Locate every blood parasite and identify its species.
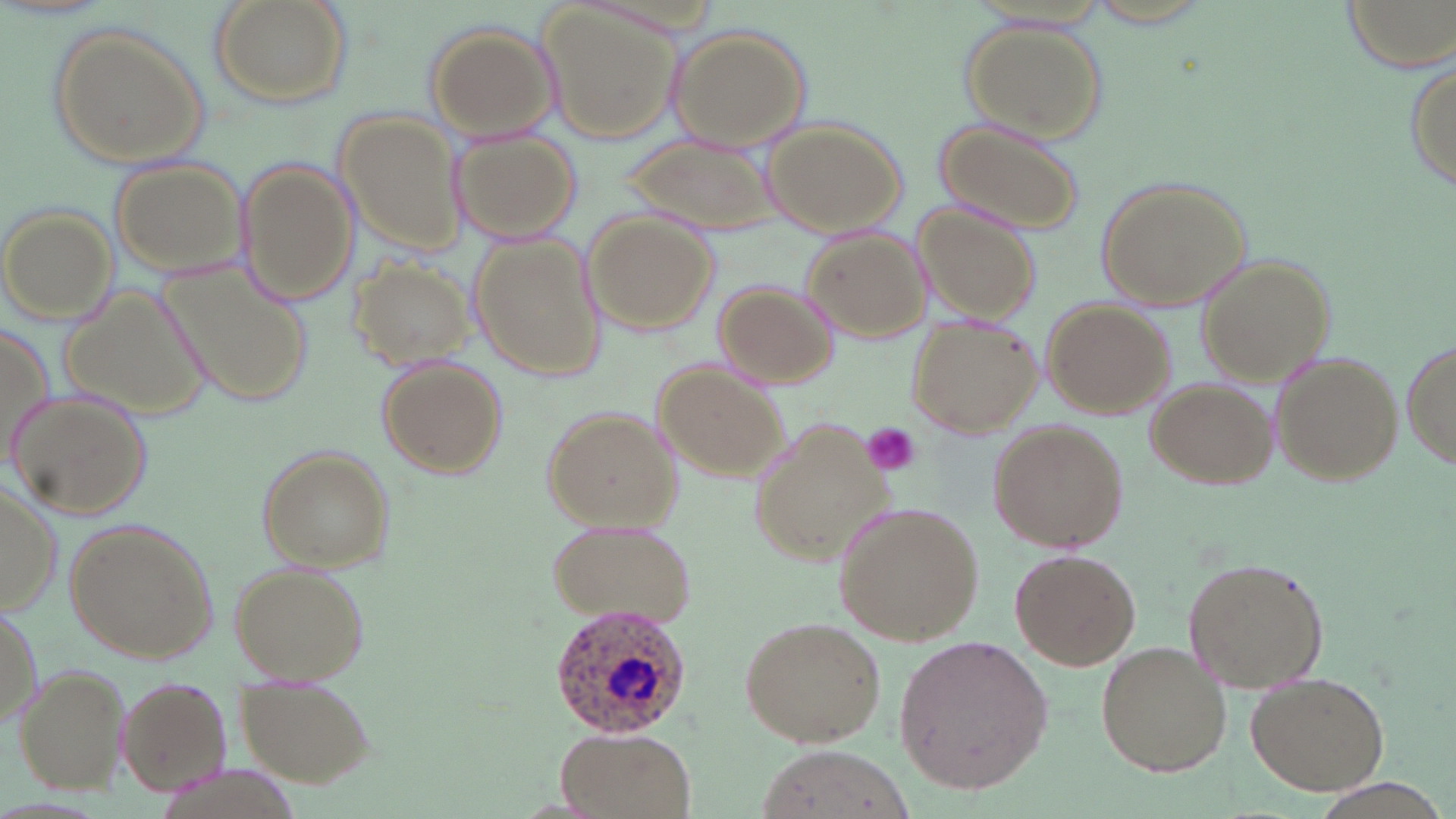
Approximate bounding boxes as [x1, y1, x2, y2] in pixels.
Plasmodium ovale-infected red blood cells: [545, 602, 693, 744].
No Plasmodium falciparum, Plasmodium malariae, Plasmodium vivax, Babesia divergens, or Trypanosoma brucei observed.

slide-level diagnosis = Plasmodium ovale
magnification = 1000x
stain = May-Grünwald-Giemsa
image size = 1456×819 pixels
uninfected red blood cell locations = approximate bounding boxes as [x1, y1, x2, y2] in pixels: [210, 0, 352, 109], [1338, 0, 1454, 72], [541, 5, 681, 144], [961, 18, 1105, 141], [424, 23, 561, 142], [51, 24, 209, 170], [668, 26, 813, 153], [1406, 55, 1454, 200], [337, 111, 467, 257], [762, 119, 906, 238], [938, 119, 1084, 234], [451, 127, 580, 244], [617, 131, 779, 233], [108, 158, 248, 277], [236, 158, 359, 308], [1096, 177, 1250, 313], [913, 201, 1043, 326], [2, 206, 118, 324], [583, 212, 718, 334], [800, 227, 927, 343], [471, 234, 608, 381], [154, 252, 316, 408], [1197, 256, 1336, 388], [348, 257, 478, 369], [713, 279, 838, 388], [58, 281, 213, 424], [1045, 299, 1172, 416], [906, 316, 1040, 438], [1, 323, 54, 468], [1401, 340, 1456, 472], [1271, 352, 1401, 486], [377, 357, 508, 480], [652, 360, 785, 483], [1148, 378, 1277, 488], [8, 388, 152, 519], [542, 406, 684, 532], [746, 420, 885, 563], [990, 423, 1129, 552], [256, 445, 393, 573], [0, 482, 60, 618], [831, 499, 985, 648], [546, 518, 697, 631], [63, 519, 218, 666], [1009, 550, 1141, 670], [1182, 557, 1329, 693], [229, 561, 370, 686], [0, 604, 41, 735], [737, 615, 885, 749], [893, 635, 1055, 793], [1095, 640, 1233, 776], [13, 662, 131, 791], [1245, 671, 1390, 794], [234, 674, 376, 788], [114, 675, 233, 795], [553, 727, 698, 819], [754, 746, 916, 819]
modality = light microscopy
preparation = thin blood smear
field of view = single
platelet locations = approximate bounding boxes as [x1, y1, x2, y2] in pixels: [860, 424, 922, 478]